State which parasite is depicted.
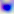

Toxoplasma gondii.

Captured at 400x magnification. Photomicrograph.